Describe the morphology of the erythrocytes.
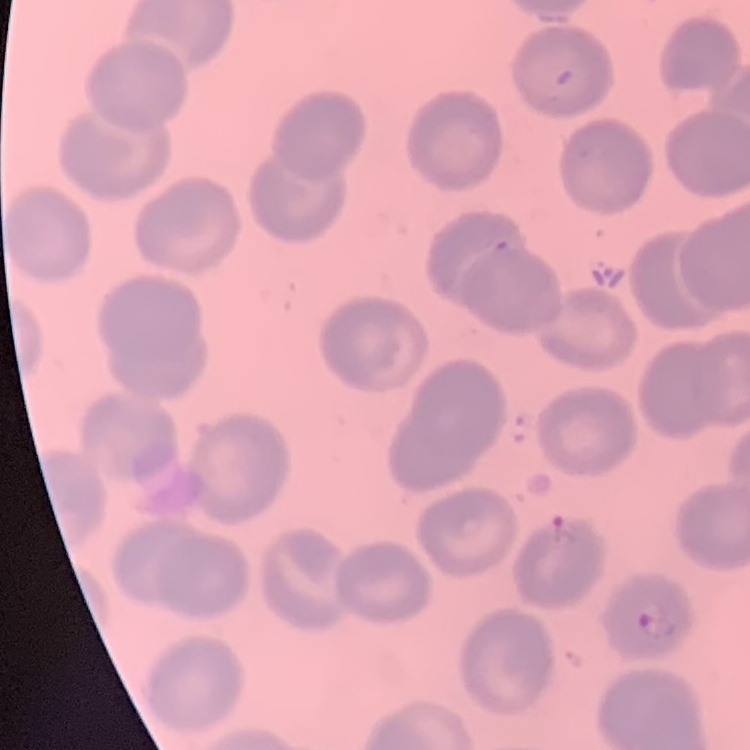
No rouleaux formation.

Thin blood smear. Field's or Giemsa stain. One tile cut from a larger photomicrograph.